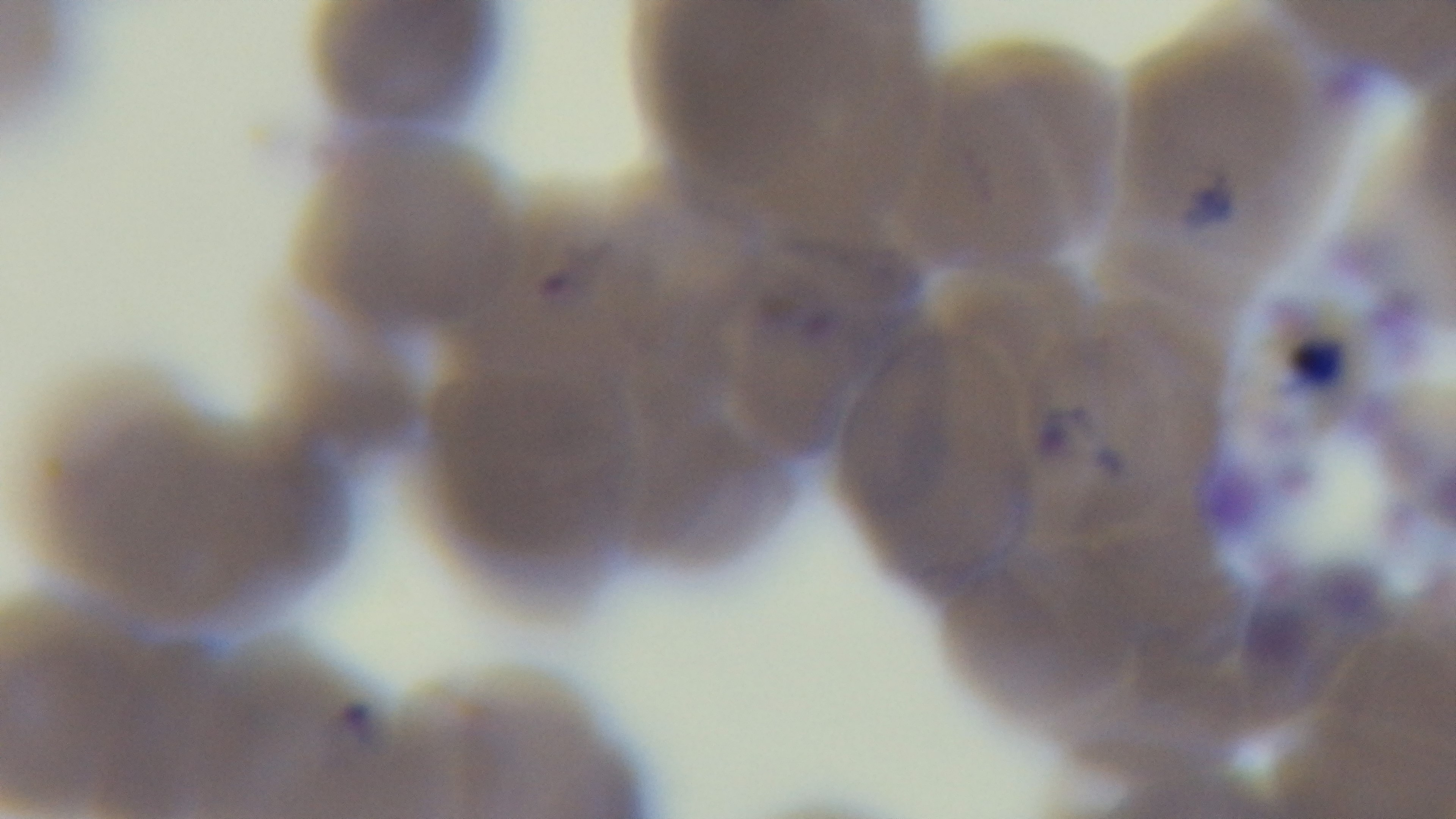

Summary:
  - Preparation: thin blood film
  - Malaria status: positive
  - Stain: Giemsa
  - Capture: mounted 4K digital camera
  - Modality: light microscopy
  - Objective: 100x oil immersion
  - Field of view: one from the slide